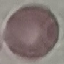

Summary:
  - Result: negative for malaria parasites
  - Stain: Giemsa
  - Capture: smartphone through the microscope eyepiece
  - Image type: cell patch, automatically extracted from a larger field of view and resized to 64 × 64 pixels
  - Preparation: thin smear